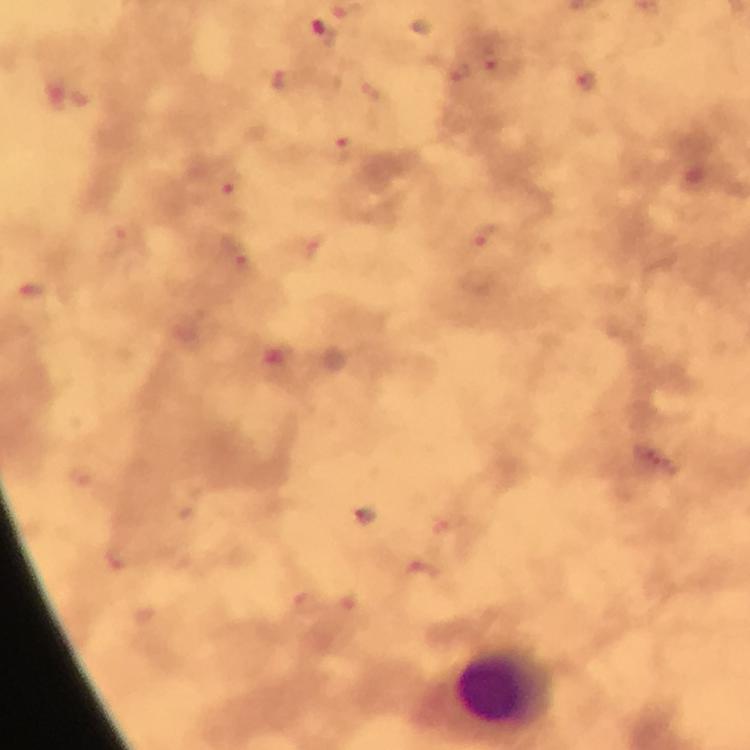

immersion oil = applied
stain = Giemsa
malaria parasite locations = approximate centers as {x, y} in pixels: {495, 62}, {459, 72}, {278, 78}, {585, 83}, {342, 146}, {228, 183}, {482, 237}, {119, 240}, {313, 246}, {236, 253}, {365, 517}
capture = smartphone camera through the microscope
magnification = 100x
cropped from = a single field of view
image size = 750×750 pixels
context = from a malaria diagnostic workup
leukocyte locations = approximate centers as {x, y} in pixels: {504, 688}
preparation = thick smear